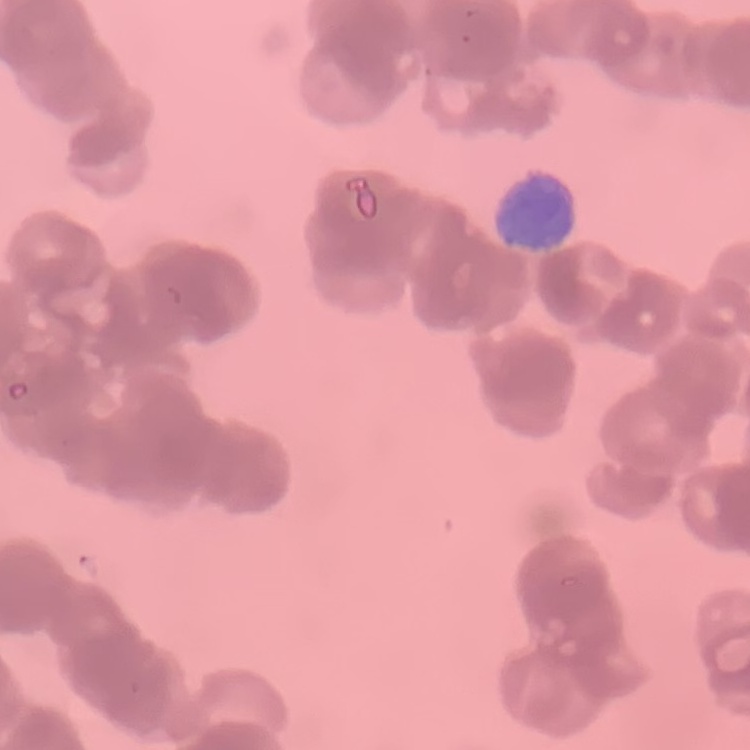
Summary:
  - Erythrocyte morphology: rouleaux formation
  - Stain: Field's or Giemsa
  - Preparation: thin peripheral smear
  - Image type: square crop of a larger photomicrograph